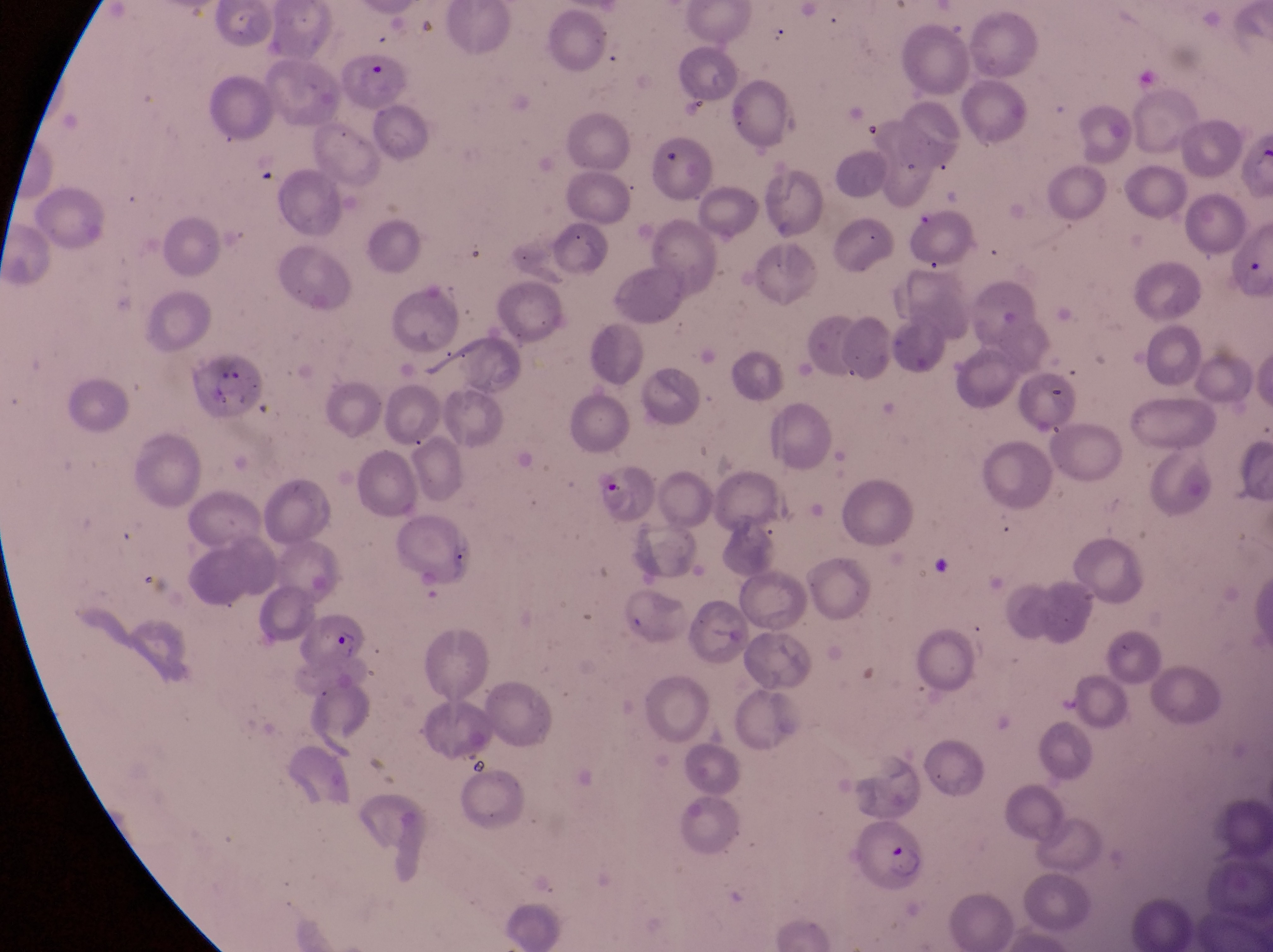
Approximate bounding boxes as (left, top, right, bottom) in pixels.
Summary:
  - Artifact (platelet-like body, stain precipitate, or debris) locations: (1043, 379, 1075, 412), (928, 552, 963, 592), (624, 607, 652, 639)
  - Parasitised red blood cell locations: (180, 348, 263, 418), (589, 460, 659, 530), (297, 605, 372, 673), (854, 826, 926, 896)
  - Preparation: thin blood smear
  - Field of view: single
  - Image size: 1273×952 pixels
  - Magnification: 1000x
  - Capture: smartphone photograph through the eyepiece of an Olympus CX-23 microscope
  - Country: Uganda